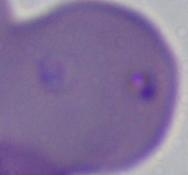
identification = Babesia
modality = photomicrograph
magnification = 1000x